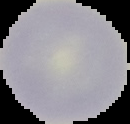

Summary:
  - Preparation: thin blood smear
  - Image size: 130×124 pixels
  - Malaria status: uninfected
  - Image type: segmented cell region with the area outside set to black